Classify this cell by malaria status.
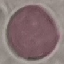

It is uninfected.

{
  "image_type": "cell patch, automatically extracted from a larger field of view and resized to 64 × 64 pixels",
  "capture": "smartphone camera at the microscope eyepiece",
  "preparation": "thin blood smear",
  "stain": "Giemsa"
}